State which cell type is depicted.
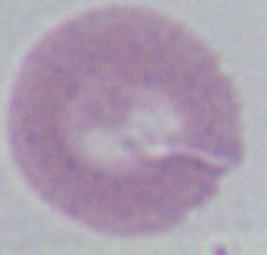

An erythrocyte.

{
  "magnification": "1000x",
  "modality": "photomicrograph"
}